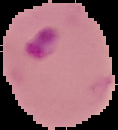 Result: Plasmodium parasites detected. From a thin blood smear. Image is 118×130 pixels. The area outside the segmented cell region is set to black.